State the blood parasite species.
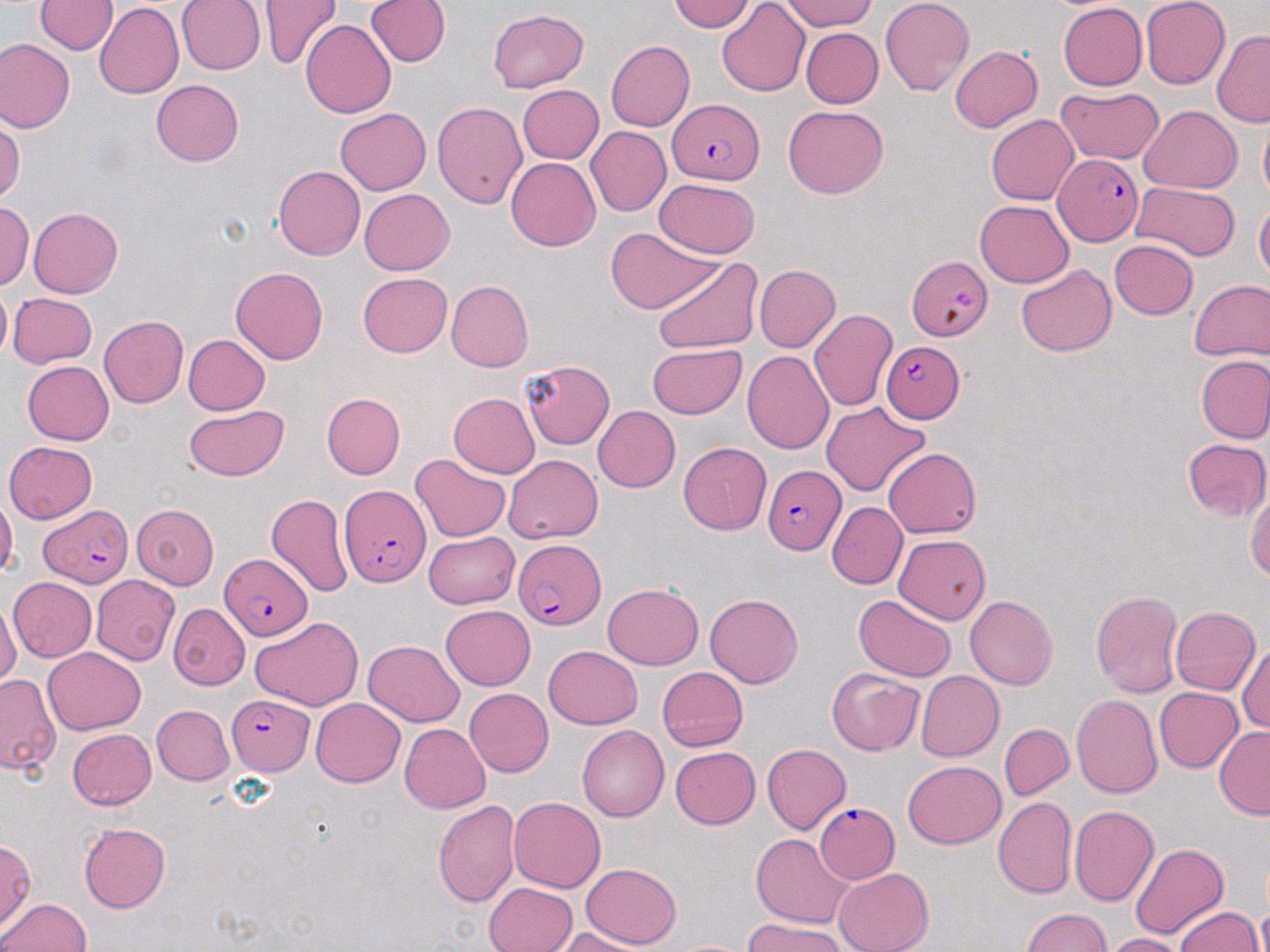
Plasmodium falciparum.

{
  "stain": "May-Grünwald-Giemsa",
  "field_of_view": "one of a larger specimen",
  "uninfected_red_blood_cell_locations": "approximate bounding boxes as [x1, y1, x2, y2] in pixels: [35, 0, 117, 55], [176, 0, 265, 75], [257, 0, 342, 71], [365, 0, 450, 68], [776, 0, 879, 31], [880, 0, 973, 97], [1140, 0, 1230, 90], [669, 1, 756, 32], [716, 1, 811, 98], [1057, 2, 1146, 91], [94, 3, 184, 99], [487, 8, 590, 93], [301, 19, 396, 118], [800, 27, 883, 109], [1211, 30, 1270, 127], [0, 40, 75, 134], [605, 40, 696, 131], [948, 46, 1043, 133], [150, 79, 244, 167], [517, 85, 604, 163], [1055, 86, 1162, 164], [432, 100, 528, 209], [783, 104, 888, 198], [1138, 106, 1241, 194], [336, 109, 431, 195], [1258, 113, 1270, 205], [986, 114, 1079, 204], [0, 117, 22, 206], [585, 126, 671, 217], [506, 157, 600, 251], [274, 166, 365, 260], [654, 178, 760, 258], [1131, 182, 1241, 260], [359, 188, 454, 275], [1254, 198, 1270, 283], [1, 200, 34, 290], [974, 200, 1074, 287], [27, 206, 123, 297], [607, 227, 720, 314], [1109, 240, 1198, 319], [653, 259, 762, 354], [753, 264, 840, 352], [1016, 265, 1117, 357], [230, 266, 328, 364], [357, 272, 452, 357], [1189, 278, 1270, 363], [445, 280, 533, 372], [0, 283, 11, 362], [8, 292, 97, 369], [807, 309, 897, 411], [99, 315, 189, 408], [183, 334, 270, 415], [646, 344, 745, 418], [742, 350, 835, 454], [1196, 356, 1270, 444], [521, 360, 614, 449], [22, 361, 113, 445], [321, 393, 405, 480], [448, 393, 541, 478], [821, 401, 930, 496], [184, 404, 290, 482], [593, 406, 681, 493], [1183, 438, 1270, 521], [4, 441, 98, 524], [678, 442, 772, 535], [884, 447, 981, 538], [409, 453, 510, 542], [503, 454, 602, 543], [1246, 488, 1270, 580], [0, 493, 18, 580], [266, 493, 352, 598], [827, 501, 908, 589], [131, 504, 220, 589], [423, 531, 520, 608], [894, 534, 991, 623], [91, 575, 179, 666], [8, 576, 96, 661], [602, 583, 704, 670], [1090, 589, 1183, 697], [704, 592, 804, 687], [853, 593, 956, 681], [964, 595, 1058, 689], [0, 603, 22, 689], [169, 603, 249, 690], [440, 605, 536, 689], [1170, 606, 1259, 696], [251, 616, 364, 710], [363, 639, 464, 726], [1235, 642, 1270, 732], [544, 645, 642, 730], [41, 647, 146, 735], [657, 667, 748, 751], [827, 667, 924, 756], [916, 671, 1003, 761], [0, 672, 60, 775], [1154, 687, 1243, 772], [465, 688, 553, 778], [1071, 694, 1161, 798], [310, 698, 405, 787], [151, 705, 234, 785], [399, 723, 491, 814], [999, 723, 1074, 800], [577, 725, 670, 822], [1213, 725, 1270, 821], [67, 729, 156, 810], [762, 744, 851, 833], [670, 747, 761, 829], [901, 761, 1006, 849], [509, 796, 605, 893], [994, 797, 1078, 898], [432, 799, 519, 908], [1068, 806, 1159, 907], [78, 823, 170, 913], [750, 834, 853, 928], [0, 838, 36, 929], [1129, 841, 1229, 942], [581, 863, 682, 948], [833, 867, 933, 952], [483, 882, 577, 951], [1, 897, 90, 951], [1256, 904, 1270, 952], [1174, 906, 1262, 952], [1020, 907, 1112, 952], [743, 919, 846, 952], [555, 927, 654, 952], [1102, 933, 1189, 952], [668, 939, 755, 951]",
  "preparation": "thin blood smear",
  "image_size": "1270×952 pixels",
  "magnification": "1000x",
  "modality": "optical microscopy",
  "plasmodium_falciparum_infected_red_blood_cell_locations": "approximate bounding boxes as [x1, y1, x2, y2] in pixels: [668, 98, 765, 185], [1053, 154, 1141, 245], [906, 256, 991, 341], [880, 340, 964, 423], [763, 466, 844, 555], [338, 484, 430, 591], [40, 505, 132, 586], [514, 538, 603, 630], [219, 553, 311, 640], [226, 693, 312, 778], [815, 802, 900, 884]"
}